Name the parasite shown.
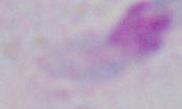
This is Toxoplasma gondii.

Summary:
  - Magnification: 1000x
  - Modality: micrograph